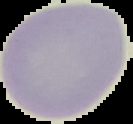

Summary:
  - Preparation: thin blood smear
  - Result: no malaria parasites seen
  - Image type: segmented cell region with the area outside set to black
  - Image size: 133×124 pixels